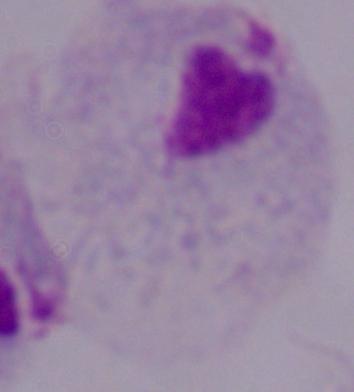

Captured at 1000x magnification. Micrograph. A trichomonad is seen.